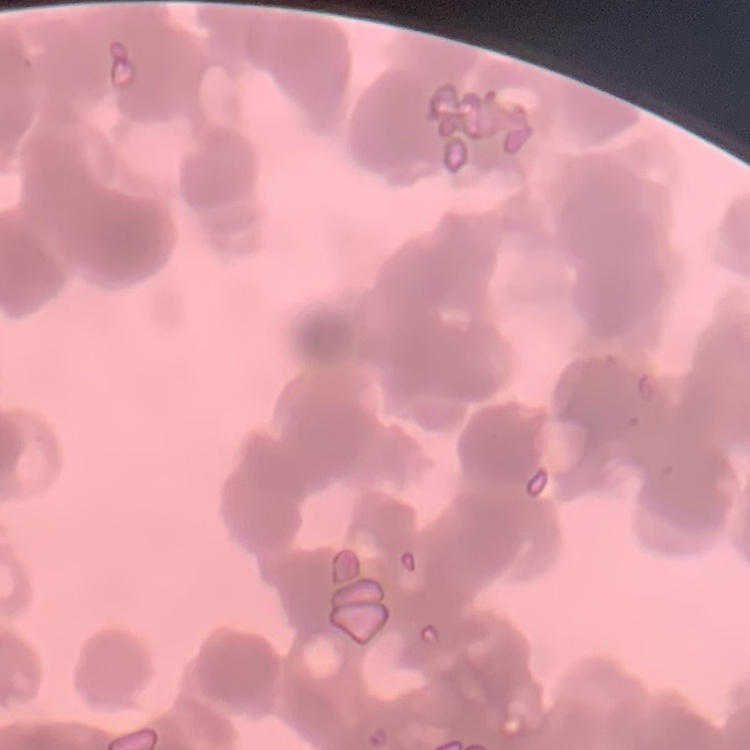

Summary:
  - Red blood cell morphology: rouleaux formation
  - Preparation: thin blood film
  - Image type: square crop of a larger photomicrograph
  - Stain: Field's or Giemsa